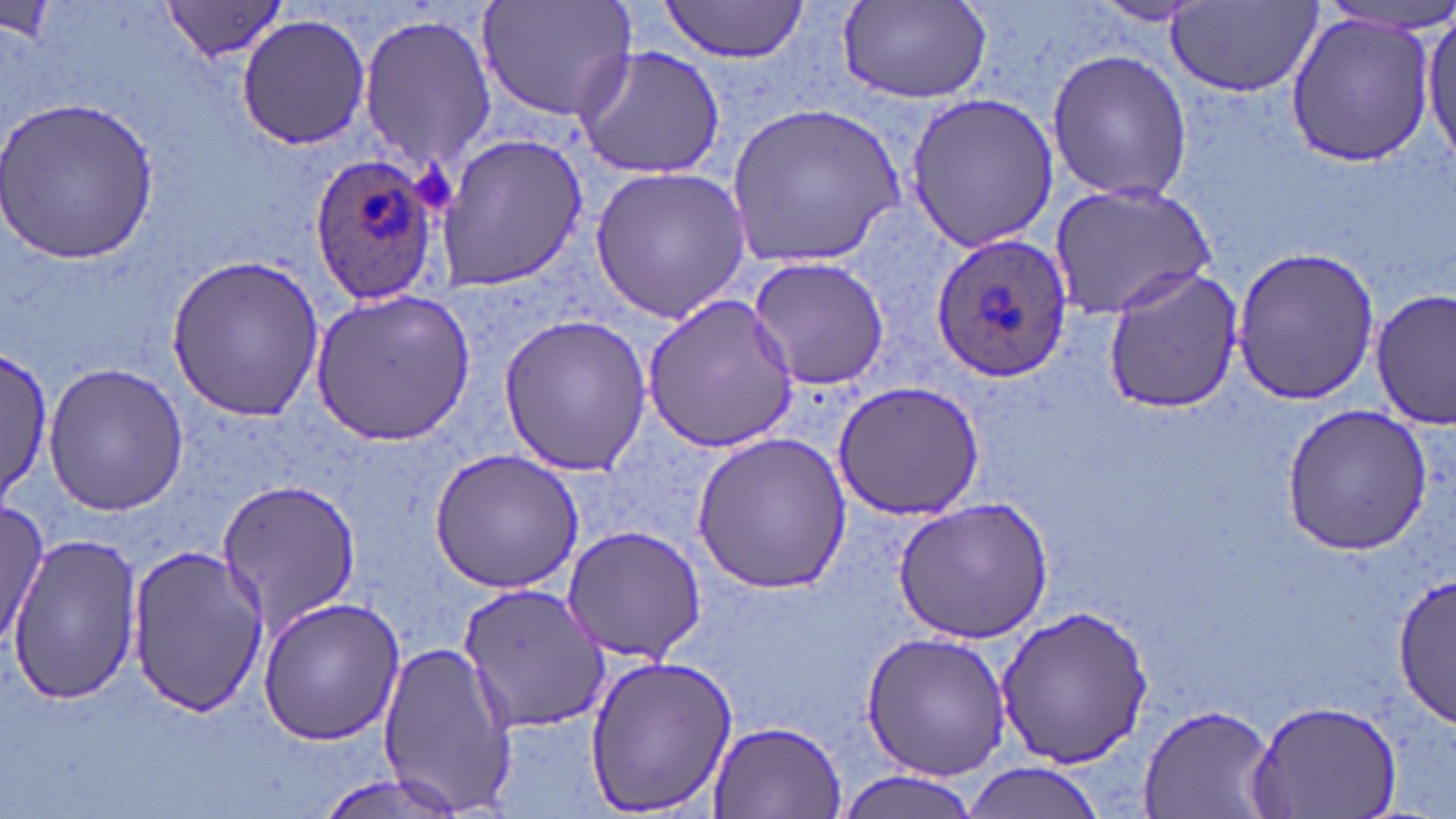

slide-level diagnosis = Plasmodium ovale
uninfected red blood cell locations = approximate bounding boxes as (x1,y1)-(x2,y2) corner pairs in pixels: (476,0)-(638,125), (658,0)-(814,63), (161,2)-(292,63), (838,2)-(992,106), (1090,2)-(1208,26), (1169,3)-(1322,99), (1418,10)-(1453,166), (358,13)-(496,172), (1283,13)-(1435,163), (235,14)-(371,151), (572,44)-(728,181), (1044,48)-(1194,205), (903,92)-(1062,253), (2,95)-(162,264), (728,105)-(905,267), (436,133)-(589,294), (590,167)-(750,321), (1047,182)-(1214,320), (1231,246)-(1383,406), (166,254)-(324,423), (747,255)-(890,393), (1100,268)-(1245,414), (307,286)-(480,448), (1371,288)-(1455,429), (642,294)-(800,456), (496,313)-(652,479), (0,348)-(52,502), (42,361)-(190,517), (830,379)-(985,519), (1283,404)-(1434,553), (691,429)-(853,594), (425,449)-(584,595), (213,479)-(363,637), (893,497)-(1052,645), (0,499)-(55,647), (559,525)-(707,665), (6,535)-(145,704), (124,541)-(267,720), (1392,575)-(1456,727), (456,581)-(609,736), (256,597)-(406,746), (996,604)-(1154,771), (860,630)-(1012,779), (373,641)-(517,812), (584,652)-(738,816), (1250,698)-(1404,818), (1139,702)-(1277,817), (703,718)-(848,818), (958,763)-(1108,819), (309,769)-(466,819), (834,772)-(984,818)
stain = May-Grünwald-Giemsa
Plasmodium ovale-infected red blood cell locations = approximate bounding boxes as (x1,y1)-(x2,y2) corner pairs in pixels: (307,154)-(445,308), (929,230)-(1073,384)
magnification = 1000x
preparation = thin blood film
image size = 1456×819 pixels
field of view = single
modality = optical microscopy
platelet locations = approximate bounding boxes as (x1,y1)-(x2,y2) corner pairs in pixels: (416,162)-(455,212)